Evaluate for Plasmodium parasites.
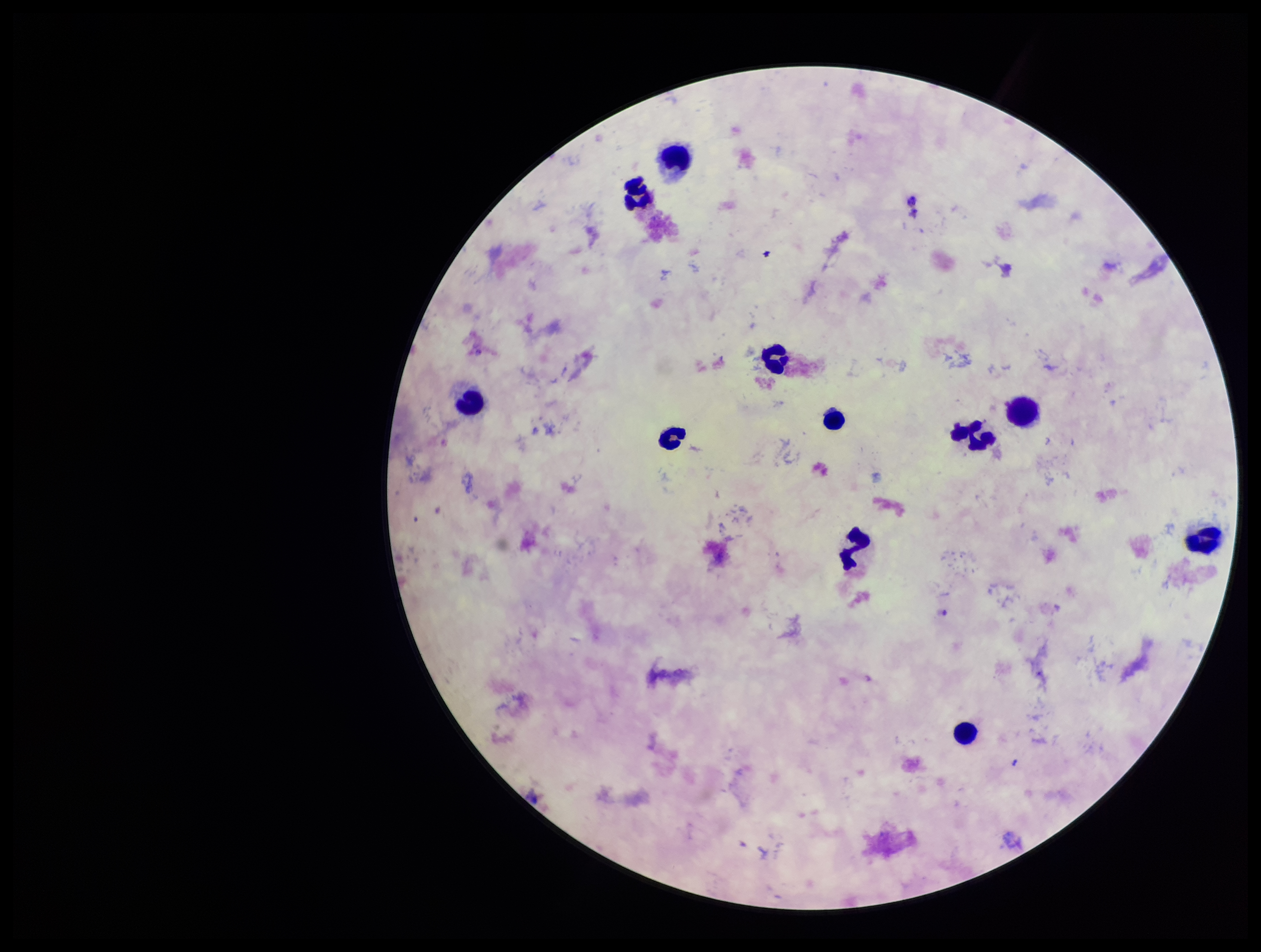
None identified.

Preparation: thick blood smear. Single field of view. Leukocyte count: 11. Species reported for this patient: Plasmodium falciparum. Image is 1261×952 pixels. Parasite count: 0. Smartphone photograph taken through the eyepiece of a microscope. Patient malaria status: infected. Giemsa stain.